Classify the preparation.
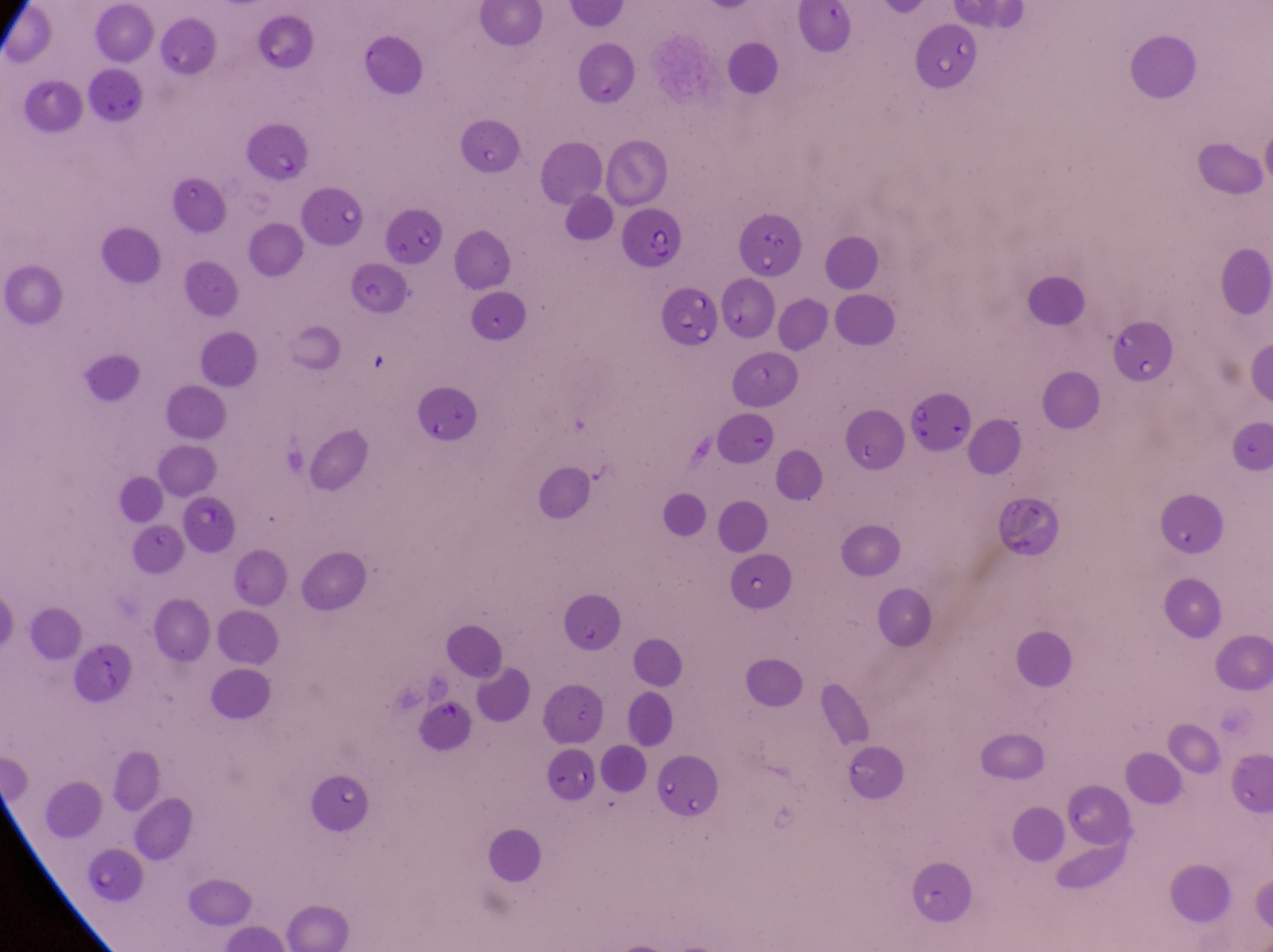
Thin blood film.

Approximate bounding boxes as left top right bottom in pixels. Parasitised red blood cell locations: 248 122 313 185; 621 212 686 270; 344 264 411 317; 654 285 717 353; 1109 324 1179 386; 904 389 981 463. Artifact (platelet-like body, stain precipitate, or debris) locations: 430 687 465 726. Image is 1273×952 pixels. Collected in Uganda. One field of view. Captured by a smartphone held over the eyepiece of an Olympus CX-23 microscope. Magnification of 1000x.